Locate every blood parasite and identify its species.
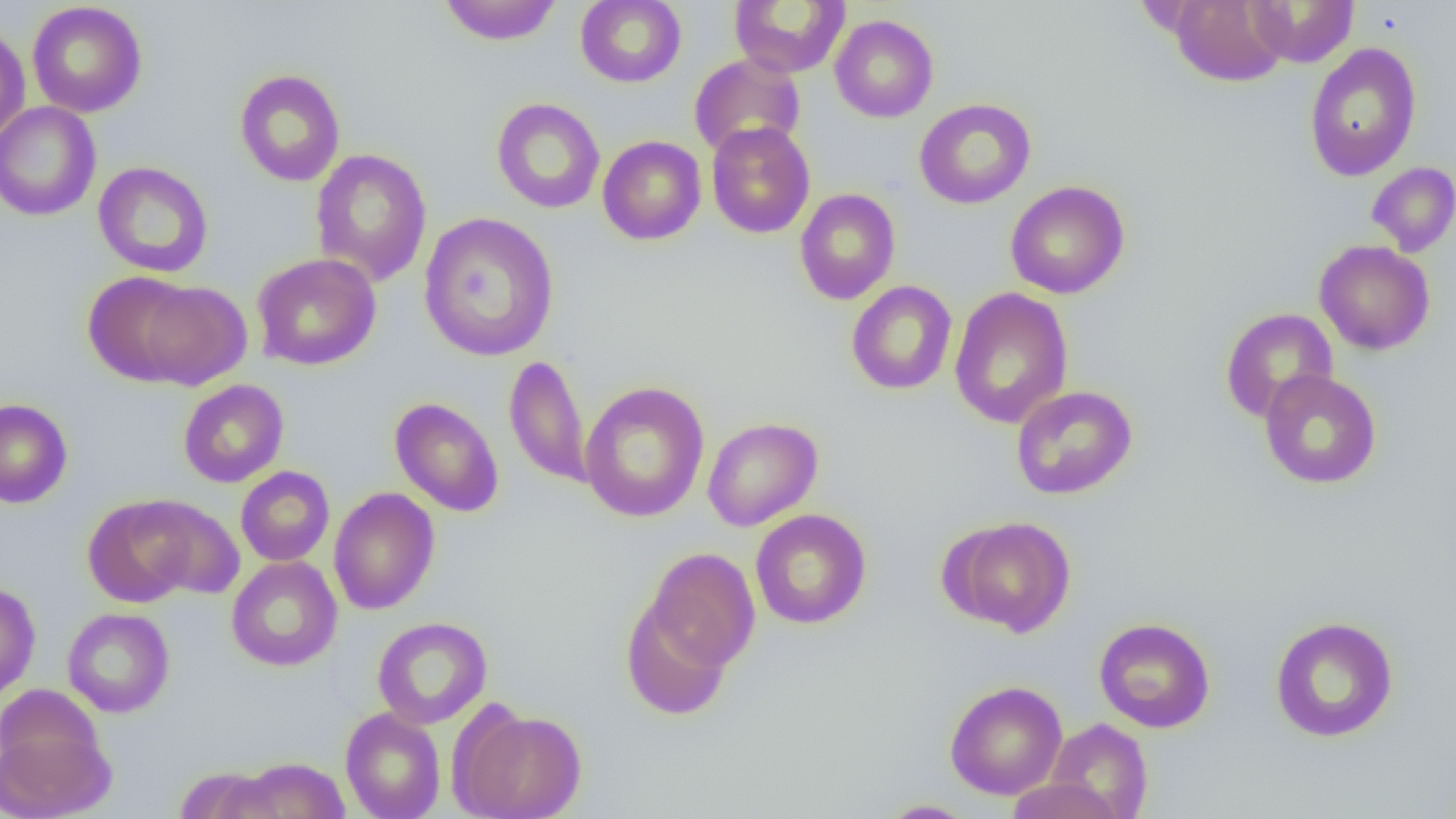
No blood parasites observed.

Approximate bounding boxes as named x1/y1/x2/y2 corners in pixels. Uninfected red blood cell locations: (x1=438, y1=0, x2=562, y2=45), (x1=575, y1=0, x2=687, y2=88), (x1=729, y1=0, x2=851, y2=78), (x1=1170, y1=0, x2=1289, y2=88), (x1=1246, y1=0, x2=1359, y2=68), (x1=27, y1=2, x2=147, y2=118), (x1=829, y1=14, x2=939, y2=123), (x1=0, y1=24, x2=30, y2=145), (x1=1303, y1=42, x2=1422, y2=181), (x1=689, y1=54, x2=805, y2=159), (x1=234, y1=69, x2=346, y2=186), (x1=491, y1=97, x2=605, y2=213), (x1=914, y1=98, x2=1036, y2=209), (x1=0, y1=102, x2=101, y2=222), (x1=707, y1=122, x2=815, y2=239), (x1=598, y1=136, x2=706, y2=245), (x1=310, y1=148, x2=432, y2=287), (x1=93, y1=161, x2=214, y2=278), (x1=1366, y1=162, x2=1456, y2=257), (x1=1005, y1=180, x2=1130, y2=299), (x1=794, y1=188, x2=901, y2=305), (x1=419, y1=212, x2=559, y2=363), (x1=1314, y1=240, x2=1435, y2=355), (x1=251, y1=252, x2=381, y2=371), (x1=82, y1=271, x2=201, y2=386), (x1=136, y1=279, x2=252, y2=390), (x1=845, y1=280, x2=958, y2=395), (x1=949, y1=286, x2=1073, y2=429), (x1=1220, y1=307, x2=1338, y2=424), (x1=504, y1=355, x2=592, y2=488), (x1=1259, y1=369, x2=1382, y2=489), (x1=178, y1=379, x2=289, y2=488), (x1=578, y1=380, x2=710, y2=523), (x1=1011, y1=385, x2=1138, y2=500), (x1=390, y1=397, x2=504, y2=517), (x1=0, y1=398, x2=73, y2=509), (x1=702, y1=417, x2=823, y2=531), (x1=235, y1=466, x2=335, y2=566), (x1=328, y1=487, x2=440, y2=615), (x1=84, y1=495, x2=203, y2=608), (x1=136, y1=497, x2=245, y2=599), (x1=750, y1=509, x2=872, y2=629), (x1=944, y1=515, x2=1076, y2=637), (x1=643, y1=547, x2=761, y2=676), (x1=226, y1=556, x2=342, y2=671), (x1=0, y1=582, x2=40, y2=701), (x1=620, y1=595, x2=736, y2=721), (x1=62, y1=607, x2=175, y2=718), (x1=372, y1=616, x2=492, y2=729), (x1=1269, y1=616, x2=1399, y2=743), (x1=1094, y1=617, x2=1215, y2=733), (x1=944, y1=680, x2=1068, y2=800), (x1=340, y1=707, x2=446, y2=819), (x1=453, y1=707, x2=587, y2=819), (x1=1045, y1=717, x2=1153, y2=818), (x1=0, y1=725, x2=114, y2=819), (x1=237, y1=757, x2=349, y2=818), (x1=174, y1=765, x2=282, y2=819), (x1=1003, y1=778, x2=1126, y2=818), (x1=876, y1=799, x2=979, y2=818). Slide-level diagnosis: no evidence of blood parasites. Captured at 1000x magnification. Thin blood smear. Optical microscopy. Image is 1456×819 pixels. Single field of view.